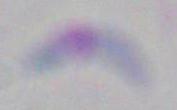
magnification = 1000x
identification = Toxoplasma gondii
modality = photomicrograph